Classify this cell by malaria status.
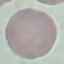
It is uninfected.

Giemsa-stained preparation. Acquired by smartphone through the microscope eyepiece. Automatically extracted cell patch, resized to 64 × 64 pixels. Thin blood film.